Give the extent of all Plasmodium falciparum-infected red blood cells.
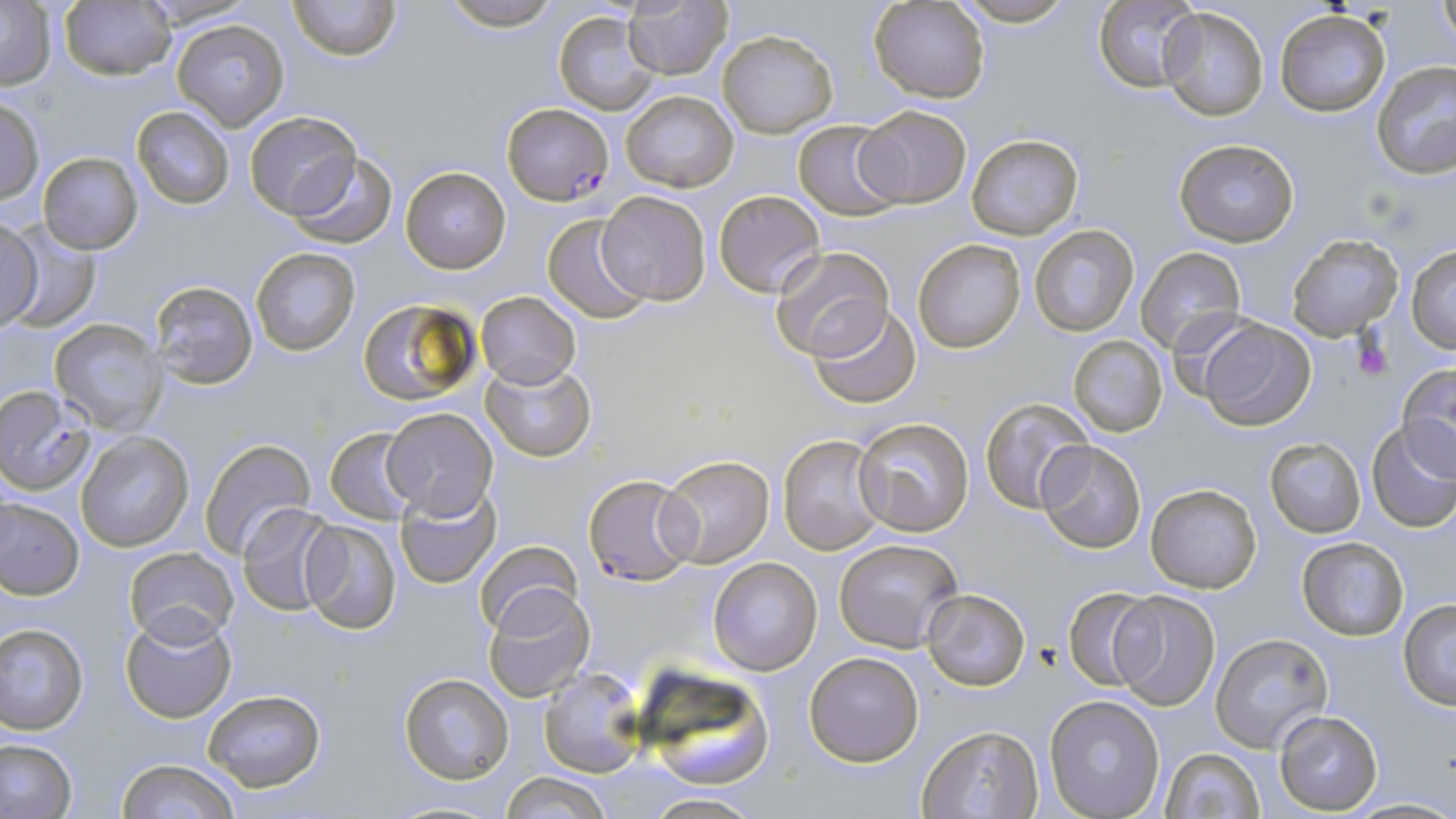
Approximate bounding boxes as [x1, y1, x2, y2] in pixels.
Plasmodium falciparum-infected red blood cells: [502, 102, 612, 205], [0, 387, 93, 496], [584, 474, 699, 588].

{
  "slide_level_diagnosis": "Plasmodium falciparum",
  "uninfected_red_blood_cell_locations": "approximate bounding boxes as [x1, y1, x2, y2] in pixels: [133, 0, 256, 28], [289, 0, 400, 60], [441, 0, 563, 30], [953, 0, 1077, 27], [1093, 0, 1200, 91], [1436, 0, 1455, 50], [1, 1, 55, 90], [60, 1, 174, 80], [869, 1, 991, 102], [623, 2, 731, 79], [1156, 5, 1269, 121], [554, 9, 661, 115], [1274, 12, 1390, 117], [172, 20, 286, 129], [717, 29, 837, 137], [1372, 62, 1456, 182], [619, 89, 739, 192], [1, 96, 45, 205], [854, 105, 973, 208], [131, 106, 235, 209], [243, 110, 361, 221], [793, 119, 905, 220], [966, 133, 1084, 240], [1173, 139, 1300, 246], [286, 150, 398, 248], [39, 152, 143, 254], [401, 166, 510, 273], [713, 189, 826, 297], [596, 190, 711, 306], [541, 214, 652, 323], [0, 217, 43, 329], [2, 224, 99, 333], [1028, 224, 1140, 335], [1286, 236, 1402, 340], [913, 238, 1027, 354], [1406, 246, 1456, 353], [252, 247, 359, 355], [767, 247, 895, 363], [1136, 247, 1247, 356], [150, 280, 258, 389], [476, 291, 580, 388], [358, 297, 481, 406], [810, 304, 923, 408], [1196, 316, 1316, 430], [50, 318, 163, 434], [1068, 334, 1168, 438], [481, 361, 596, 461], [1396, 364, 1456, 476], [980, 397, 1096, 514], [381, 407, 498, 518], [854, 417, 975, 535], [1366, 422, 1456, 533], [325, 428, 421, 525], [78, 431, 193, 551], [778, 434, 886, 555], [200, 437, 316, 558], [1265, 437, 1366, 537], [1037, 439, 1146, 553], [657, 454, 775, 569], [1145, 483, 1261, 593], [396, 484, 501, 587], [0, 498, 84, 598], [237, 503, 341, 614], [298, 519, 402, 635], [835, 538, 963, 651], [1296, 538, 1409, 641], [473, 541, 581, 639], [124, 546, 241, 647], [708, 557, 821, 675], [482, 585, 595, 703], [1062, 586, 1162, 692], [922, 588, 1030, 691], [1110, 589, 1221, 711], [1397, 600, 1456, 710], [120, 609, 237, 723], [0, 624, 89, 734], [1209, 633, 1334, 754], [804, 649, 926, 767], [633, 666, 778, 788], [540, 667, 645, 776], [399, 673, 514, 784], [201, 688, 326, 791], [1043, 694, 1166, 818], [1274, 710, 1383, 813], [916, 724, 1045, 818], [0, 737, 76, 819], [1160, 746, 1266, 819], [115, 757, 242, 818], [502, 772, 609, 819], [640, 792, 764, 818], [1344, 797, 1456, 817]",
  "modality": "optical microscopy",
  "platelet_locations": "approximate bounding boxes as [x1, y1, x2, y2] in pixels: [1354, 334, 1393, 381]",
  "stain": "May-Grünwald-Giemsa",
  "preparation": "thin blood smear",
  "image_size": "1456×819 pixels",
  "field_of_view": "single",
  "magnification": "1000x"
}